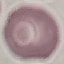
Result: no malaria parasites detected. Photographed with a smartphone camera at the microscope eyepiece. Automatically extracted cell patch, resized to 64 × 64 pixels. Thin smear of blood. Giemsa stain.